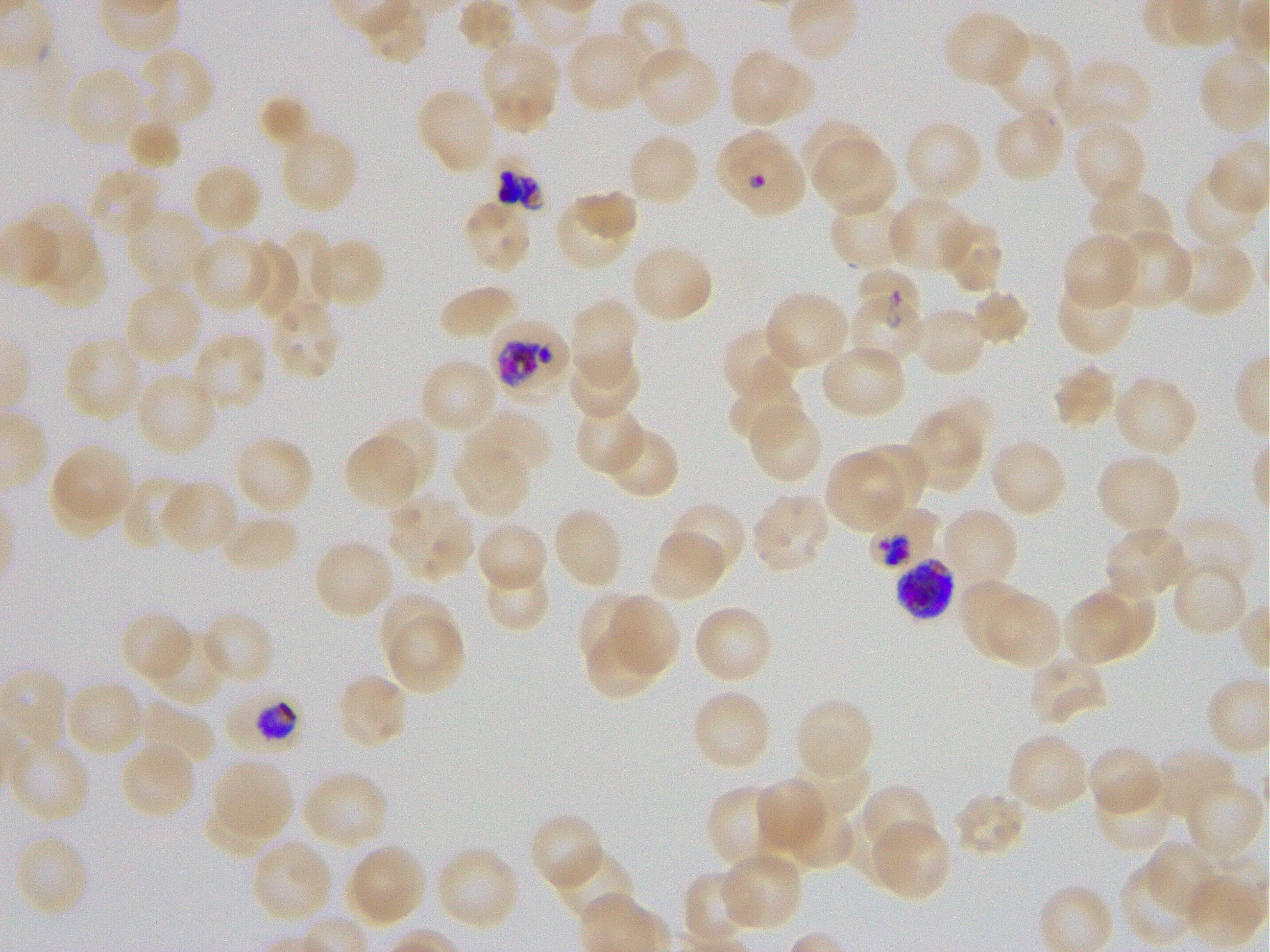
Approximate bounding boxes as [x1, y1, x2, y2] in pixels. Not every red blood cell is marked. A life-cycle stage — or a range of stages, where the recorded stages span more than one — follows each staged infected red blood cell. Locations of red blood cells of indeterminate infection status: [848, 296, 925, 366]. Locations of infected red blood cells: [714, 128, 806, 218]; [496, 166, 543, 210]; [859, 268, 922, 329] early ring to early trophozoite; [488, 318, 571, 399] late trophozoite to early schizont; [866, 504, 938, 571]; [895, 557, 957, 620]; [224, 685, 304, 753] trophozoite. Locations of uninfected red blood cells: [942, 9, 1030, 90], [565, 28, 649, 114], [988, 31, 1074, 119], [481, 40, 559, 105], [634, 45, 721, 127], [137, 47, 215, 128], [728, 48, 813, 127], [1064, 57, 1154, 133], [66, 67, 144, 147], [483, 80, 557, 135], [415, 87, 496, 176], [258, 95, 315, 151], [993, 105, 1067, 184], [125, 112, 182, 173], [802, 118, 873, 189], [903, 119, 984, 202], [1073, 121, 1147, 206], [279, 130, 359, 214], [626, 131, 701, 207], [815, 139, 896, 216], [190, 163, 263, 234], [85, 167, 161, 239], [1182, 169, 1261, 250], [1087, 187, 1173, 257], [573, 190, 637, 242], [554, 192, 637, 269], [829, 197, 912, 269], [889, 197, 976, 273], [461, 201, 534, 273], [26, 207, 88, 285], [125, 209, 208, 293], [941, 219, 1004, 293], [1113, 229, 1195, 310], [274, 230, 338, 314], [191, 233, 271, 312], [1060, 233, 1142, 310], [317, 237, 387, 309], [1173, 238, 1256, 318], [242, 242, 301, 319], [42, 243, 110, 310], [629, 243, 714, 325], [1054, 278, 1137, 356], [438, 283, 521, 343], [122, 284, 202, 365], [970, 288, 1030, 346], [764, 289, 850, 371], [569, 297, 639, 386], [268, 298, 341, 381], [913, 307, 989, 377], [721, 325, 802, 403], [191, 333, 268, 413], [62, 335, 144, 422], [820, 342, 907, 420], [568, 350, 641, 422], [418, 357, 499, 435], [1050, 362, 1118, 430], [134, 371, 218, 455], [1113, 374, 1198, 456], [728, 378, 805, 446], [936, 398, 992, 455], [746, 402, 821, 484], [574, 403, 648, 475], [468, 409, 552, 480], [908, 410, 982, 490], [372, 415, 439, 490], [600, 424, 679, 499], [343, 434, 420, 508], [233, 435, 315, 515], [988, 439, 1069, 518], [453, 443, 532, 518], [855, 443, 925, 519], [57, 445, 134, 518], [825, 450, 906, 532], [1096, 453, 1182, 536], [49, 467, 121, 533], [121, 476, 194, 552], [160, 479, 238, 554], [752, 492, 830, 575], [386, 495, 472, 581], [667, 502, 748, 580], [552, 506, 625, 590], [940, 507, 1019, 588], [220, 511, 301, 574], [1168, 518, 1256, 590], [475, 521, 549, 595], [1103, 525, 1189, 602], [648, 531, 725, 601], [312, 539, 394, 619], [1172, 560, 1249, 638], [482, 565, 552, 633], [1085, 578, 1154, 658], [958, 579, 1031, 657], [1063, 590, 1132, 663], [377, 592, 455, 665], [577, 592, 654, 670], [607, 594, 680, 677], [987, 595, 1060, 667], [693, 604, 774, 684], [199, 609, 276, 685], [119, 611, 195, 683], [387, 612, 464, 694], [147, 628, 226, 708], [584, 628, 664, 701], [1027, 655, 1108, 726], [336, 673, 409, 751], [65, 679, 144, 758], [690, 688, 773, 772], [794, 696, 874, 779], [136, 700, 215, 771], [1005, 733, 1089, 814], [9, 736, 91, 824], [119, 741, 196, 820], [1086, 744, 1164, 816], [1156, 745, 1239, 820], [790, 752, 870, 819], [212, 758, 292, 840], [302, 770, 389, 849], [755, 778, 829, 855], [1094, 778, 1173, 852], [1186, 778, 1264, 864], [863, 784, 937, 851], [707, 785, 787, 873], [952, 790, 1028, 860], [203, 799, 279, 859], [784, 801, 855, 871], [838, 804, 920, 888], [529, 812, 605, 892], [869, 818, 951, 902], [13, 833, 90, 918], [250, 838, 333, 924], [1146, 841, 1221, 920], [346, 842, 426, 927], [435, 844, 520, 930], [553, 846, 633, 922], [718, 851, 805, 931], [1119, 862, 1195, 946], [683, 872, 755, 947]. Giemsa stain. Oil immersion, 100x objective (numerical aperture 1.25). Single field of view. Plasmodium falciparum strain 3D7 in static in-vitro culture. Thin blood film. Blood group of the donor: O+. Image is 1270×952 pixels.